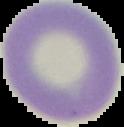
Summary:
  - Image type: segmented cell region with the area outside set to black
  - Preparation: thin blood film
  - Image size: 124×127 pixels
  - Result: negative for malaria parasites